Locate and identify every blood parasite.
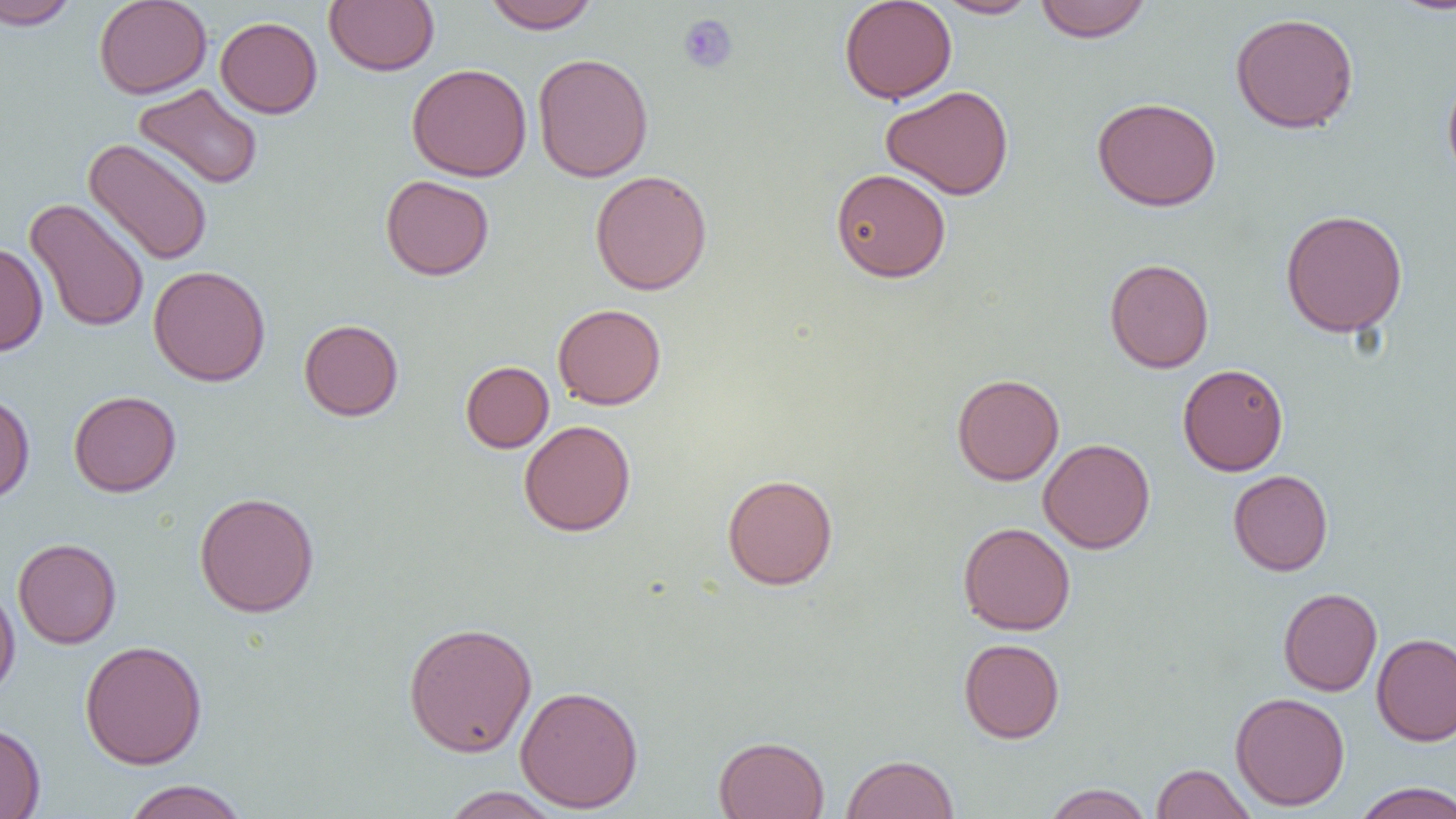

No blood parasites observed.

Approximate bounding boxes as (x1,y1)-(x2,y2) corner pairs in pixels. Uninfected red blood cell locations: (0,0)-(80,30), (94,0)-(212,99), (324,0)-(439,75), (482,0)-(601,33), (839,0)-(957,104), (934,0)-(1042,18), (1386,0)-(1456,16), (1034,1)-(1152,43), (1230,12)-(1360,134), (215,16)-(322,118), (532,53)-(653,182), (406,64)-(532,181), (1442,69)-(1456,186), (133,83)-(264,190), (881,85)-(1014,200), (1092,97)-(1222,211), (83,138)-(213,266), (830,168)-(951,282), (589,170)-(713,295), (381,174)-(494,281), (24,197)-(150,333), (1280,208)-(1408,338), (0,241)-(48,356), (1104,258)-(1214,373), (148,265)-(271,386), (553,303)-(666,410), (299,318)-(404,421), (461,361)-(554,453), (1177,363)-(1289,476), (951,373)-(1064,485), (68,390)-(182,497), (0,391)-(35,506), (519,420)-(636,536), (1038,438)-(1155,553), (1228,470)-(1333,576), (721,473)-(838,590), (194,491)-(320,617), (958,522)-(1076,635), (13,538)-(121,649), (0,581)-(20,702), (1278,587)-(1382,696), (402,621)-(538,757), (1371,633)-(1456,746), (958,638)-(1065,743), (80,639)-(207,769), (515,685)-(644,813), (1230,692)-(1350,811), (0,721)-(46,818), (714,735)-(830,819), (841,753)-(959,819), (1150,763)-(1256,819), (121,779)-(249,819), (1351,782)-(1456,819), (1042,783)-(1154,819), (438,786)-(565,818). Platelet locations: (678,13)-(738,74). Slide-level diagnosis: negative for blood parasites. Captured at 1000x magnification. One field of a larger specimen. Thin blood film. Optical microscopy. Image is 1456×819 pixels.